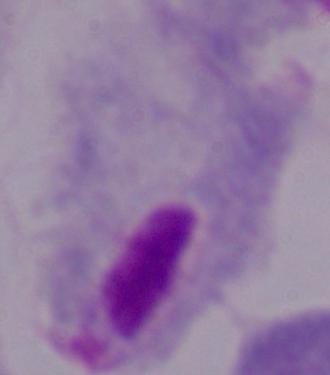
1000x magnification. A trichomonad is shown. Micrograph.